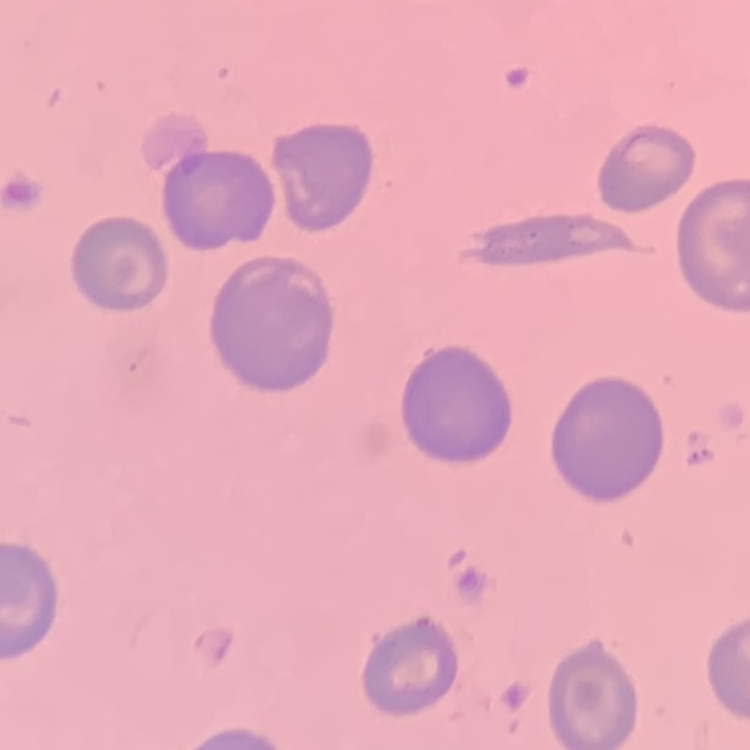

The erythrocytes exhibit no rouleaux formation. One tile cut from a larger photomicrograph. Thin blood smear. Field's or Giemsa stain.